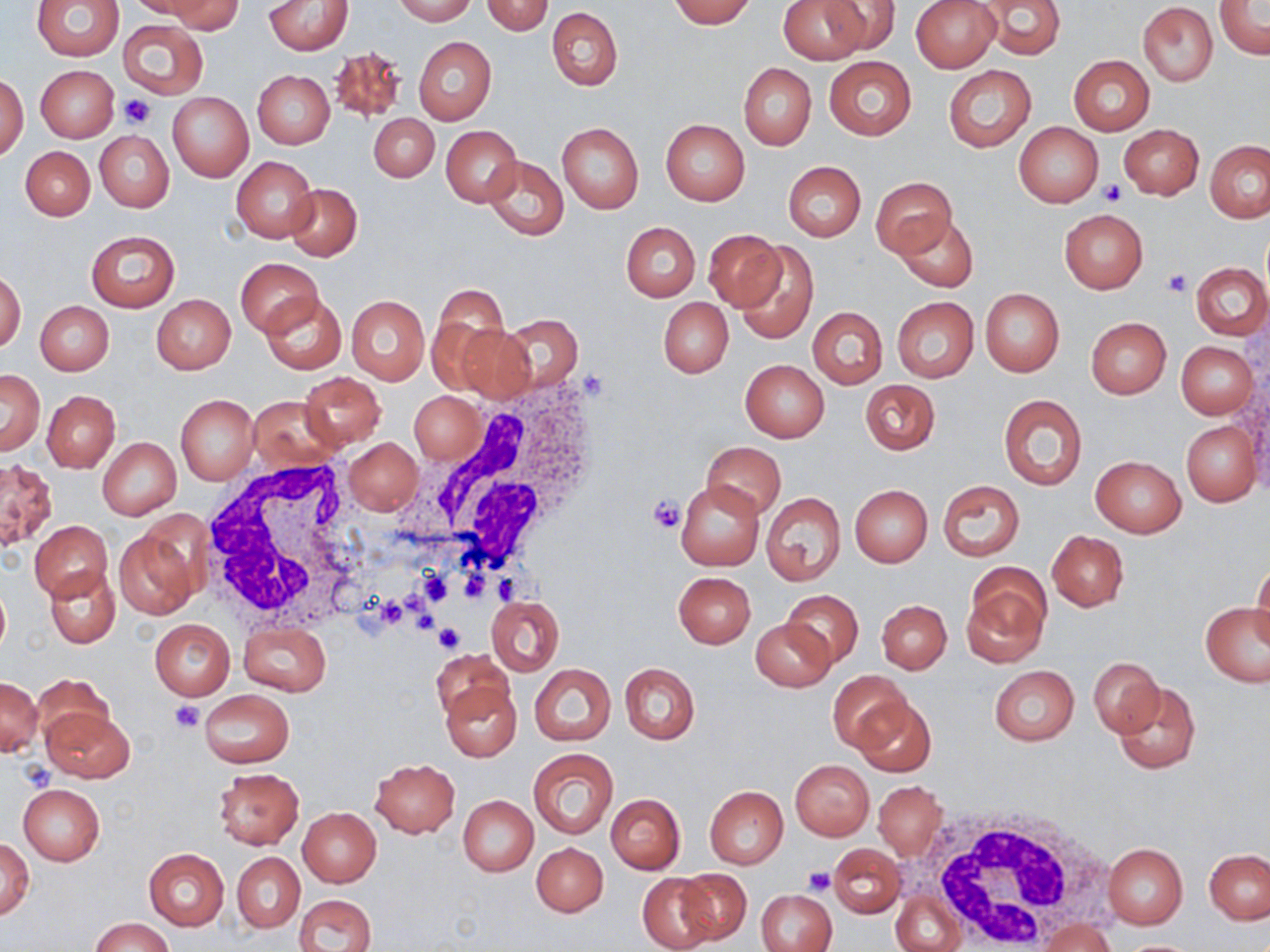
Approximate bounding boxes as (x1,y1)-(x2,y2) corner pairs in pixels. Uninfected red blood cell locations: (33,0)-(124,60), (126,0)-(217,18), (393,0)-(477,24), (668,0)-(756,27), (779,0)-(868,64), (911,0)-(1001,72), (981,0)-(1067,59), (161,1)-(242,34), (264,1)-(352,54), (821,1)-(900,54), (482,2)-(553,35), (1139,2)-(1218,86), (1215,3)-(1269,59), (547,7)-(622,90), (118,19)-(208,99), (414,36)-(497,126), (328,44)-(409,123), (1068,54)-(1154,134), (823,57)-(916,139), (738,63)-(816,151), (35,65)-(118,143), (943,65)-(1036,152), (252,70)-(334,149), (1,73)-(29,160), (168,92)-(253,182), (370,113)-(438,182), (660,119)-(750,206), (557,122)-(644,214), (1013,123)-(1104,206), (1120,124)-(1204,199), (440,126)-(522,206), (95,131)-(174,212), (1205,141)-(1270,223), (21,146)-(95,220), (483,155)-(567,240), (231,156)-(317,242), (784,162)-(866,241), (869,177)-(957,257), (286,184)-(361,260), (1059,208)-(1148,293), (894,212)-(978,292), (622,222)-(700,301), (85,230)-(180,311), (703,230)-(783,310), (731,240)-(819,344), (235,258)-(323,336), (1191,263)-(1269,341), (1,271)-(25,353), (430,286)-(511,379), (980,288)-(1064,377), (260,291)-(346,374), (152,294)-(235,374), (346,295)-(429,384), (891,296)-(979,383), (659,299)-(732,377), (36,300)-(113,376), (807,307)-(887,389), (499,313)-(584,392), (1085,316)-(1172,398), (456,326)-(535,402), (1177,342)-(1257,418), (740,360)-(828,442), (0,369)-(44,455), (297,371)-(386,451), (860,379)-(940,454), (43,390)-(119,472), (410,391)-(483,464), (248,394)-(344,472), (176,395)-(258,484), (999,395)-(1087,489), (1181,421)-(1260,507), (97,438)-(181,519), (343,438)-(423,516), (702,441)-(786,519), (1091,456)-(1185,537), (0,459)-(56,550), (939,480)-(1024,561), (675,481)-(763,571), (850,485)-(932,567), (761,492)-(846,584), (29,520)-(112,601), (114,528)-(199,620), (1047,531)-(1127,611), (1251,562)-(1270,651), (46,566)-(119,647), (961,568)-(1049,665), (673,571)-(756,647), (0,580)-(10,659), (781,589)-(863,669), (487,596)-(564,674), (878,600)-(951,673), (1201,603)-(1270,688), (150,619)-(235,699), (752,620)-(834,692), (238,623)-(331,696), (433,649)-(513,722), (1089,657)-(1162,736), (621,662)-(700,744), (530,663)-(616,746), (989,665)-(1079,745), (828,670)-(912,752), (33,673)-(111,745), (1,677)-(43,755), (1113,681)-(1201,774), (440,682)-(520,761), (199,689)-(294,767), (853,697)-(936,777), (42,706)-(135,782), (528,749)-(619,838), (370,758)-(460,836), (790,760)-(874,839), (214,767)-(304,850), (874,780)-(947,860), (18,783)-(105,865), (704,786)-(788,867), (606,793)-(685,873), (458,796)-(538,876), (296,807)-(381,887), (1,837)-(34,920), (532,842)-(608,917), (1103,842)-(1188,929), (829,843)-(906,918), (144,849)-(229,931), (1205,849)-(1269,924), (232,853)-(303,932), (674,869)-(752,946), (638,872)-(719,952), (759,888)-(836,952), (891,890)-(965,952), (295,893)-(376,952), (1038,917)-(1118,951), (89,918)-(174,952), (1118,939)-(1205,952). White blood cell locations: (418,380)-(605,576), (199,457)-(369,634), (917,800)-(1111,950). Platelet locations: (121,95)-(154,127), (1100,181)-(1127,205), (1162,268)-(1190,296), (648,495)-(684,532), (416,569)-(451,606), (458,571)-(495,601), (492,572)-(526,605), (400,587)-(431,616), (380,598)-(406,629), (413,610)-(438,632), (434,624)-(465,653), (170,698)-(204,732), (20,761)-(56,792), (804,867)-(837,895). Slide-level diagnosis: no evidence of blood parasites. 1000x magnification. One field of a larger specimen. Image is 1270×952 pixels. Light microscopy. May-Grünwald-Giemsa-stained preparation. Thin blood smear.